Describe the morphology of the red blood cells.
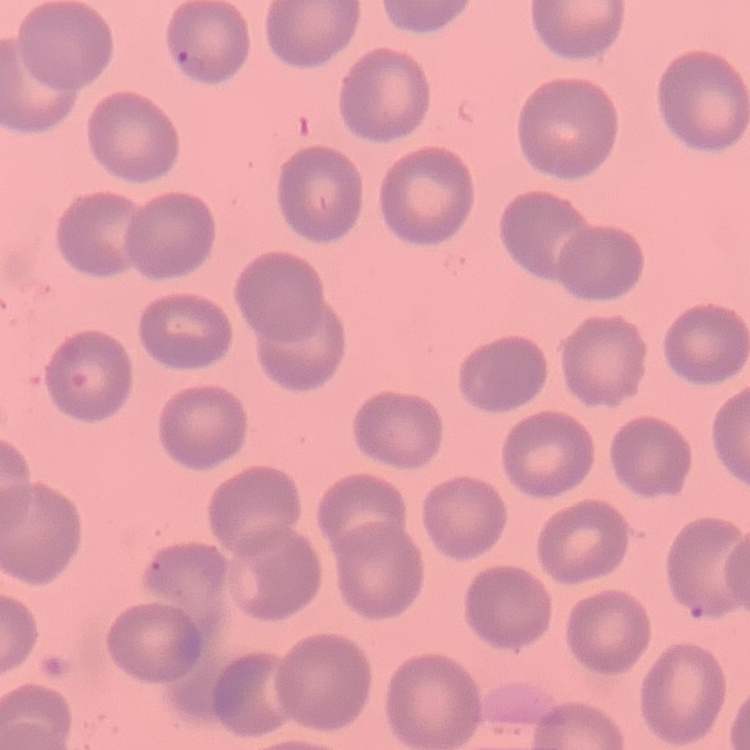
No rouleaux formation.

Summary:
  - Stain: Field's or Giemsa
  - Image type: square crop of a larger photomicrograph
  - Preparation: thin blood smear